Report the malaria status of this cell.
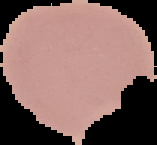
It is uninfected.

From a thin blood film. Image is 157×145 pixels. The area outside the segmented cell region is set to black.